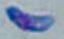

magnification = 1000x
modality = photomicrograph
identification = Toxoplasma gondii